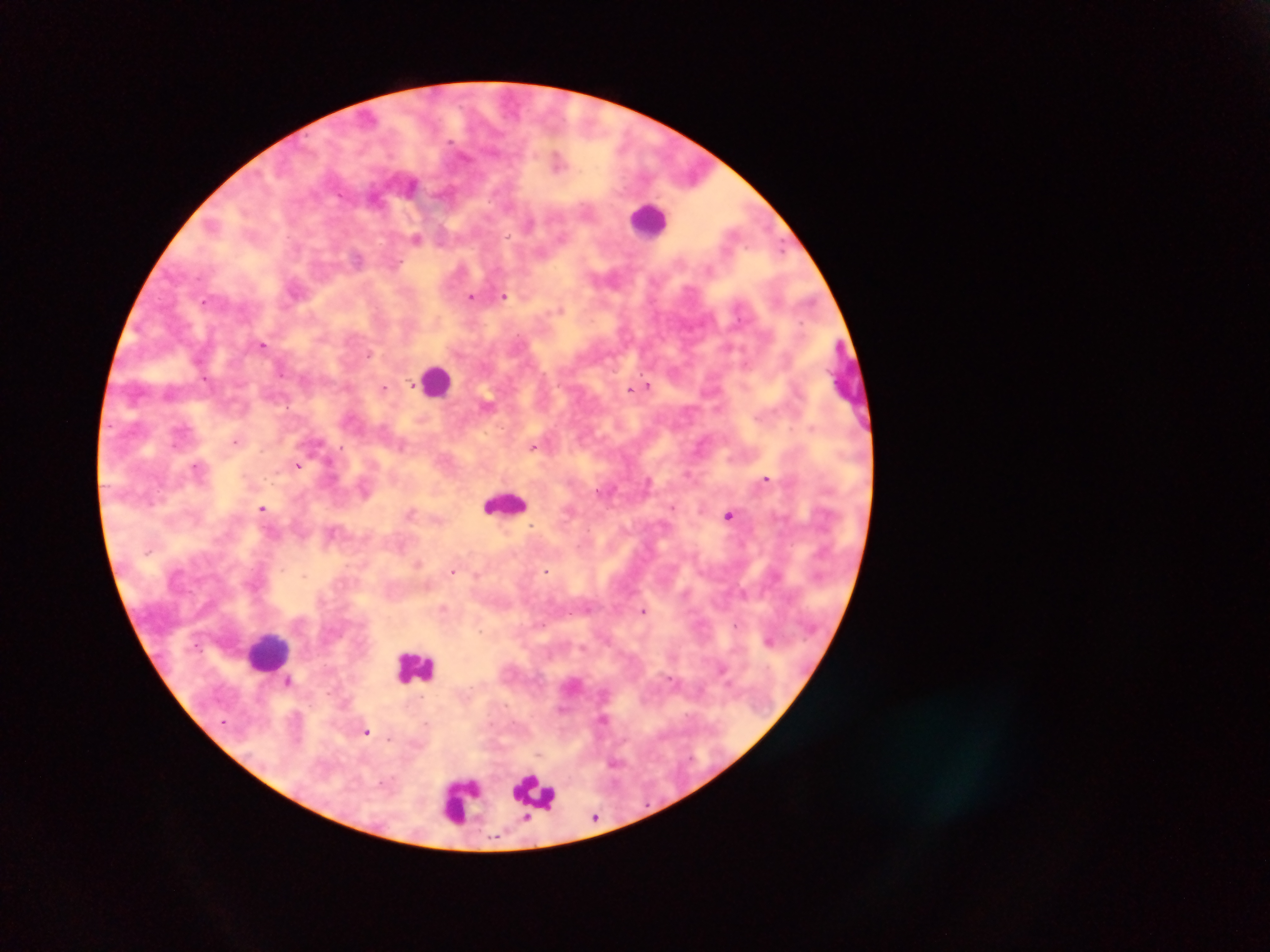

plasmodium_parasite_locations: 'approximate centers as {x, y} in pixels: {557, 161}, {412, 185}, {529, 224}, {416, 239}, {357, 258}, {503, 296}, {471, 297}, {204, 301}, {561, 309}, {263, 344}, {729, 347}, {368, 355}, {745, 365}, {280, 370}, {412, 385}, {648, 385}, {638, 387}, {384, 388}, {630, 389}, {487, 404}, {235, 441}, {402, 445}, {532, 447}, {298, 465}, {197, 467}, {765, 479}, {672, 507}, {262, 508}, {410, 511}, {728, 515}, {532, 526}, {332, 532}, {418, 564}, {453, 571}, {546, 571}, {443, 607}, {644, 610}, {736, 624}, {769, 640}, {722, 670}, {289, 681}, {603, 718}, {367, 733}, {595, 817}'
image_size: 1270×952 pixels
capture: mobile-phone photograph through a microscope
preparation: thick blood smear
field_of_view: single
leukocyte_locations: 'approximate centers as {x, y} in pixels: {650, 221}, {437, 380}, {504, 502}, {269, 650}, {415, 668}, {536, 796}, {461, 799}'
country: Ghana